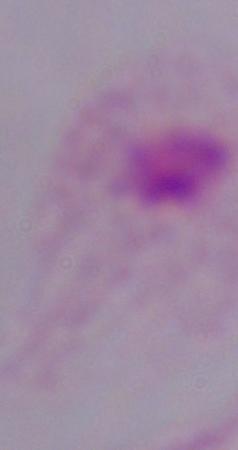
{
  "modality": "micrograph",
  "identification": "trichomonad",
  "magnification": "1000x"
}